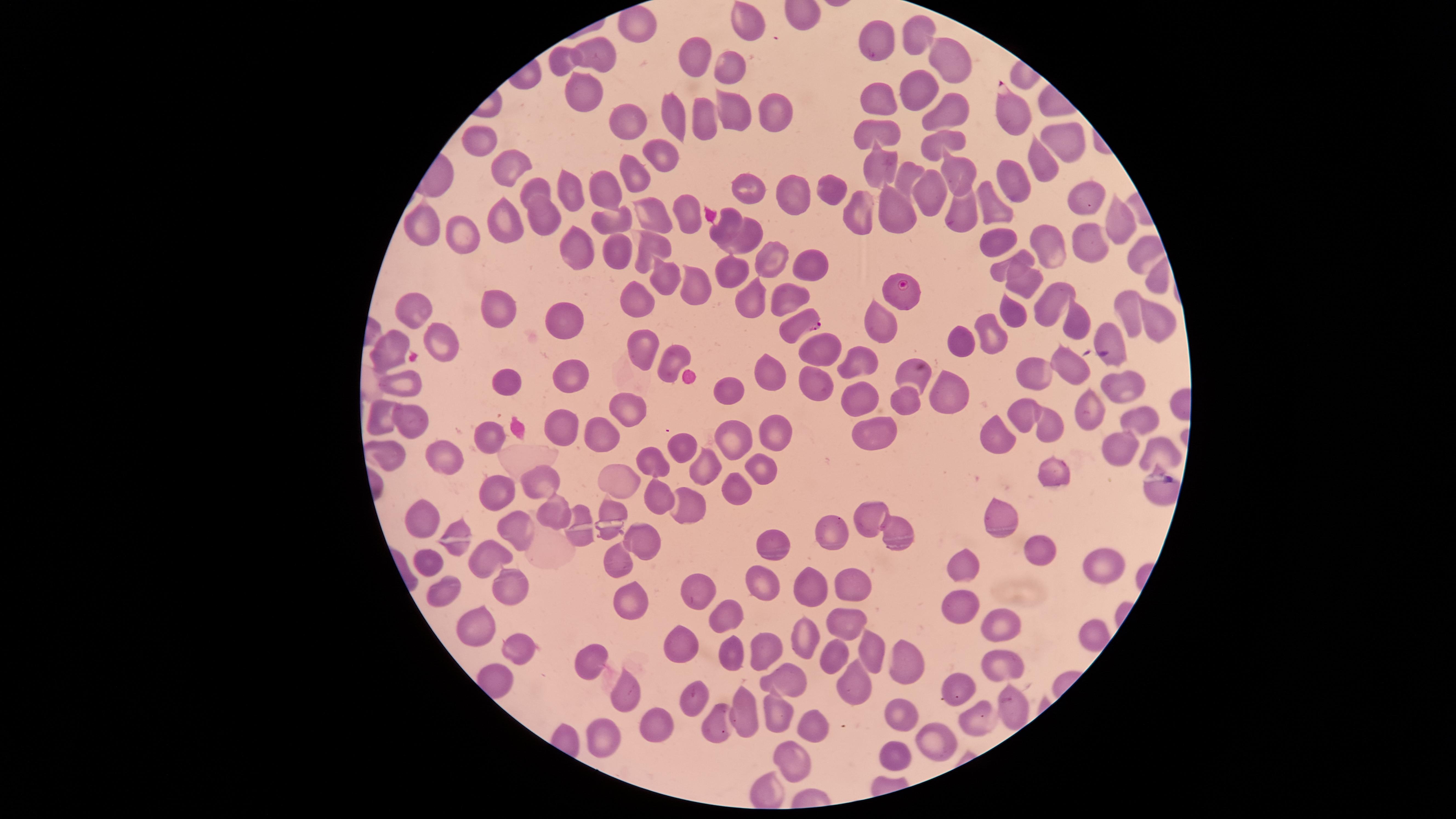

Approximate marker points as [x, y] in pixels.
Summary:
  - Uninfected red blood cells: [749, 19], [919, 33], [880, 44], [603, 56], [696, 59], [562, 60], [946, 61], [732, 67], [914, 88], [582, 91], [881, 101], [777, 110], [948, 112], [734, 113], [701, 114], [670, 117], [628, 121], [885, 133], [941, 139], [1059, 139], [482, 143], [663, 156], [506, 163], [1043, 164], [880, 167], [955, 167], [908, 172], [635, 178], [1014, 179], [533, 183], [752, 184], [606, 187], [569, 189], [826, 190], [929, 194], [1084, 197], [792, 200], [994, 204], [962, 207], [684, 210], [859, 212], [540, 215], [904, 215], [655, 216], [726, 218], [1117, 218], [608, 223], [505, 227], [424, 230], [465, 231], [750, 232], [997, 237], [652, 242], [1090, 246], [1045, 247], [1140, 248], [577, 250], [617, 253], [771, 257], [1020, 259], [808, 263], [729, 267], [663, 276], [689, 279], [1153, 279], [1027, 286], [781, 297], [750, 300], [635, 303], [1050, 303], [412, 308], [496, 311], [1016, 314], [1128, 314], [1155, 316], [563, 317], [880, 321], [1080, 321], [993, 335], [1110, 335], [443, 337], [955, 343], [641, 345], [390, 346], [824, 348], [858, 359], [670, 360], [1066, 362], [572, 372], [1034, 372], [771, 373], [915, 378], [503, 379], [397, 381], [818, 381], [1123, 383], [949, 389], [730, 390], [862, 394], [906, 394], [1091, 404], [626, 411], [1024, 412], [378, 415], [1141, 420], [412, 425], [1051, 425], [878, 427], [565, 429], [1000, 429], [496, 431], [780, 431], [599, 435], [727, 444], [1114, 444], [679, 445], [1155, 451], [389, 454], [453, 456], [702, 465], [652, 468], [757, 468], [1051, 470], [620, 478], [536, 485], [1154, 486], [737, 487], [499, 492], [658, 493], [686, 501], [551, 508], [1004, 513], [866, 515], [420, 518], [612, 523], [519, 527], [893, 529], [834, 532], [643, 538], [774, 542], [1040, 548], [488, 551], [429, 560], [618, 560], [970, 565], [1095, 565], [763, 569], [513, 580], [814, 586], [856, 586], [443, 587], [707, 589], [632, 595], [955, 605], [726, 615], [846, 620], [473, 621], [991, 621], [1082, 633], [803, 638], [684, 639], [872, 641], [518, 642], [759, 646], [732, 654], [833, 658], [907, 661], [1004, 661], [591, 662], [791, 679], [855, 685], [960, 685], [624, 688], [691, 695], [1014, 701], [739, 710], [898, 713], [979, 713], [776, 716], [814, 722], [660, 725], [721, 725], [606, 736], [930, 742], [892, 754], [794, 759], [771, 794]
  - Parasitized red blood cells: [1012, 112], [904, 290], [798, 324]
  - Presence: malaria parasites seen
  - Capture: smartphone photograph through the microscope eyepiece
  - Image size: 1456×819 pixels
  - Stain: Giemsa
  - Preparation: thin blood smear
  - Field of view: single
  - Visible region: circular
  - Species: Plasmodium falciparum